State which parasite is depicted.
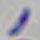
This is Toxoplasma gondii.

Photomicrograph. Captured at 1000x magnification.